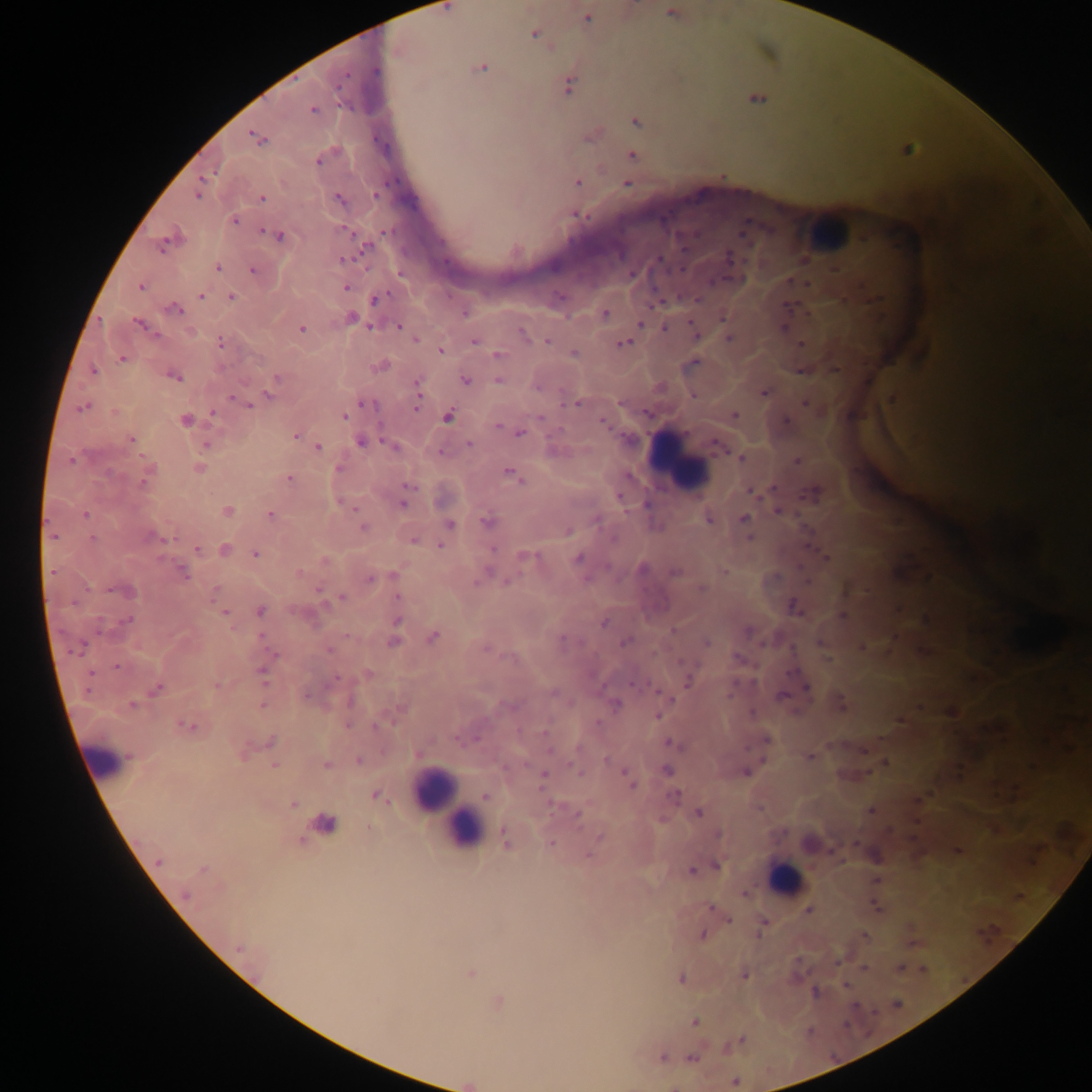

{
  "capture": "mobile-phone photograph through a microscope",
  "preparation": "thick blood smear",
  "country": "Ghana",
  "malaria_parasite_locations": "approximate centers as (x, y) in pixels: (671, 12), (589, 18), (535, 33), (482, 68), (376, 72), (569, 85), (313, 111), (635, 121), (250, 134), (631, 155), (317, 160), (579, 182), (626, 183), (375, 194), (262, 198), (578, 216), (235, 220), (266, 231), (384, 231), (279, 236), (163, 245), (365, 248), (345, 258), (660, 260), (445, 261), (218, 267), (254, 269), (682, 269), (632, 271), (140, 287), (346, 288), (229, 295), (561, 295), (200, 296), (385, 296), (699, 298), (373, 299), (653, 306), (177, 308), (604, 313), (723, 317), (99, 320), (138, 321), (690, 323), (641, 324), (399, 325), (369, 326), (665, 328), (303, 330), (522, 333), (728, 337), (415, 339), (473, 340), (221, 341), (547, 342), (623, 343), (799, 344), (439, 351), (574, 353), (495, 354), (122, 358), (93, 371), (179, 377), (277, 378), (466, 379), (497, 379), (418, 382), (418, 391), (763, 391), (268, 395), (232, 397), (239, 401), (804, 403), (249, 404), (360, 404), (563, 404), (578, 404), (83, 408), (417, 408), (213, 411), (113, 412), (734, 414), (448, 417), (344, 418), (540, 418), (788, 419), (184, 420), (604, 421), (497, 426), (519, 433), (294, 436), (132, 439), (359, 440), (383, 441), (469, 443), (205, 445), (317, 446), (715, 448), (441, 453), (143, 457), (742, 458), (797, 460), (71, 461), (338, 466), (510, 471), (516, 477), (290, 478), (143, 481), (520, 481), (408, 486), (773, 487), (752, 492), (811, 495), (339, 502), (402, 503), (354, 508), (227, 511), (777, 511), (85, 514), (268, 514), (744, 518), (708, 519), (485, 522), (450, 523), (363, 528), (568, 530), (54, 536), (749, 537), (93, 538), (171, 538), (413, 541), (440, 545), (494, 549), (196, 550), (254, 554), (826, 555), (522, 556), (537, 556), (578, 557), (725, 570), (51, 571), (180, 572), (488, 572), (300, 573), (391, 575), (586, 578), (369, 579), (506, 581), (476, 583), (318, 588), (701, 589), (111, 590), (213, 593), (397, 596), (343, 597), (793, 606), (226, 611), (261, 611), (842, 616), (128, 620), (398, 620), (604, 622), (261, 635), (346, 636), (434, 636), (563, 638), (393, 642), (624, 642), (706, 643), (760, 643), (820, 643), (83, 647), (863, 648), (486, 649), (330, 650), (73, 652), (275, 654), (736, 655), (827, 659), (117, 665), (92, 672), (262, 672), (335, 677), (687, 680), (264, 683), (632, 684), (215, 686), (807, 688), (157, 689), (87, 691), (657, 691), (306, 694), (729, 694), (783, 696), (673, 700), (840, 703), (263, 704), (616, 705), (132, 706), (920, 706), (753, 712), (659, 716), (899, 719), (390, 723), (597, 723), (346, 726), (376, 726), (189, 727), (457, 738), (478, 739), (270, 741), (666, 743), (831, 745), (747, 747), (864, 750), (548, 751), (418, 752), (243, 755), (809, 756), (359, 759), (763, 759), (606, 760), (884, 760), (526, 764), (568, 764), (275, 767), (623, 770), (667, 770), (745, 772), (544, 773), (580, 773), (632, 787), (374, 794), (485, 796), (676, 796), (293, 802), (388, 802), (550, 804), (868, 811), (699, 813), (577, 815), (659, 817), (370, 828), (719, 835), (599, 837), (549, 842), (855, 844), (831, 849), (959, 851), (589, 856), (156, 863), (716, 866), (691, 869), (744, 893), (185, 894), (875, 906), (711, 907), (809, 909), (729, 920), (764, 923), (702, 934), (758, 937), (864, 937), (912, 943), (238, 949), (796, 959), (836, 964), (864, 967), (900, 967), (923, 969), (470, 973), (744, 975), (681, 978), (845, 984), (814, 991), (694, 1022), (742, 1040), (661, 1056), (690, 1056)",
  "leukocyte_locations": "approximate centers as (x, y) in pixels: (670, 467), (113, 757), (433, 799), (462, 828), (786, 873)",
  "field_of_view": "single",
  "image_size": "1092×1092 pixels"
}